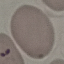
Summary:
  - Malaria status: parasitized
  - Image type: automatically extracted cell patch, resized to 64 × 64 pixels
  - Capture: smartphone camera at the microscope eyepiece
  - Preparation: thin smear
  - Stain: Giemsa